Identify the blood parasite species.
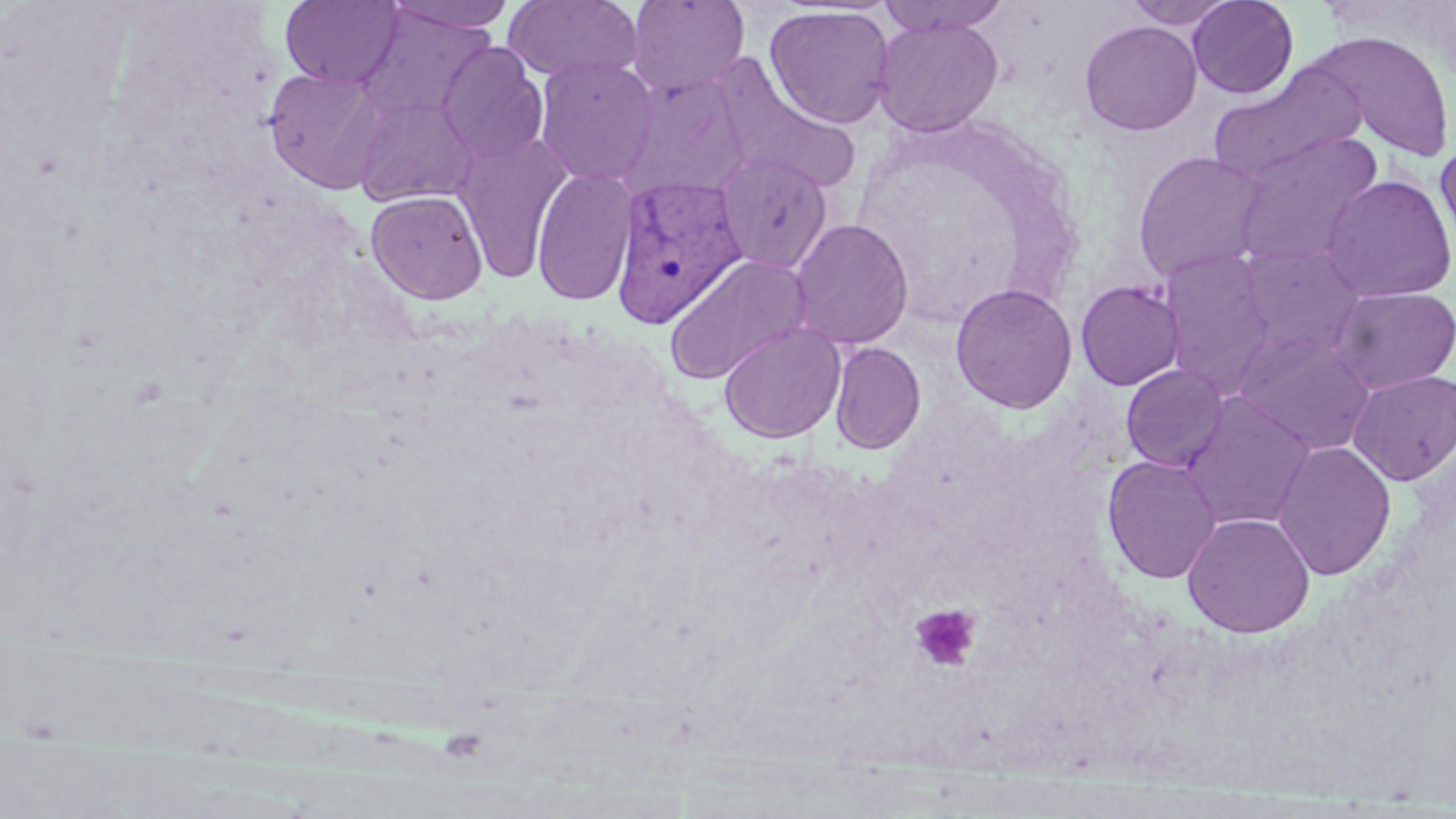
Plasmodium vivax.

platelet_locations: 'approximate bounding boxes as [x1, y1, x2, y2] in pixels: [910, 604, 981, 672]'
field_of_view: one of a larger specimen
modality: optical microscopy
magnification: 1000x
uninfected_red_blood_cell_locations: 'approximate bounding boxes as [x1, y1, x2, y2] in pixels: [280, 0, 403, 88], [387, 0, 519, 34], [627, 0, 749, 97], [874, 0, 1014, 35], [1123, 0, 1237, 29], [1186, 0, 1299, 98], [503, 1, 644, 83], [764, 4, 896, 129], [356, 5, 496, 125], [872, 16, 1003, 137], [1079, 20, 1202, 136], [1308, 31, 1456, 162], [436, 41, 549, 163], [534, 57, 659, 187], [1208, 66, 1362, 184], [713, 67, 862, 194], [264, 68, 391, 195], [354, 94, 480, 207], [451, 132, 574, 284], [1232, 132, 1385, 270], [1435, 137, 1456, 260], [1132, 150, 1268, 284], [715, 151, 834, 274], [531, 166, 638, 307], [1321, 174, 1456, 303], [366, 189, 488, 304], [789, 218, 913, 350], [1235, 243, 1368, 359], [1157, 249, 1278, 393], [663, 254, 813, 386], [1075, 280, 1186, 391], [950, 283, 1077, 414], [1328, 286, 1456, 395], [719, 321, 846, 444], [1233, 331, 1376, 455], [829, 341, 927, 455], [1121, 364, 1230, 470], [1347, 370, 1456, 485], [1179, 393, 1317, 531], [1272, 440, 1396, 580], [1102, 455, 1222, 584], [1182, 512, 1315, 637]'
stain: May-Grünwald-Giemsa
plasmodium_vivax_infected_red_blood_cell_locations: 'approximate bounding boxes as [x1, y1, x2, y2] in pixels: [609, 173, 747, 327]'
image_size: 1456×819 pixels
preparation: thin blood film